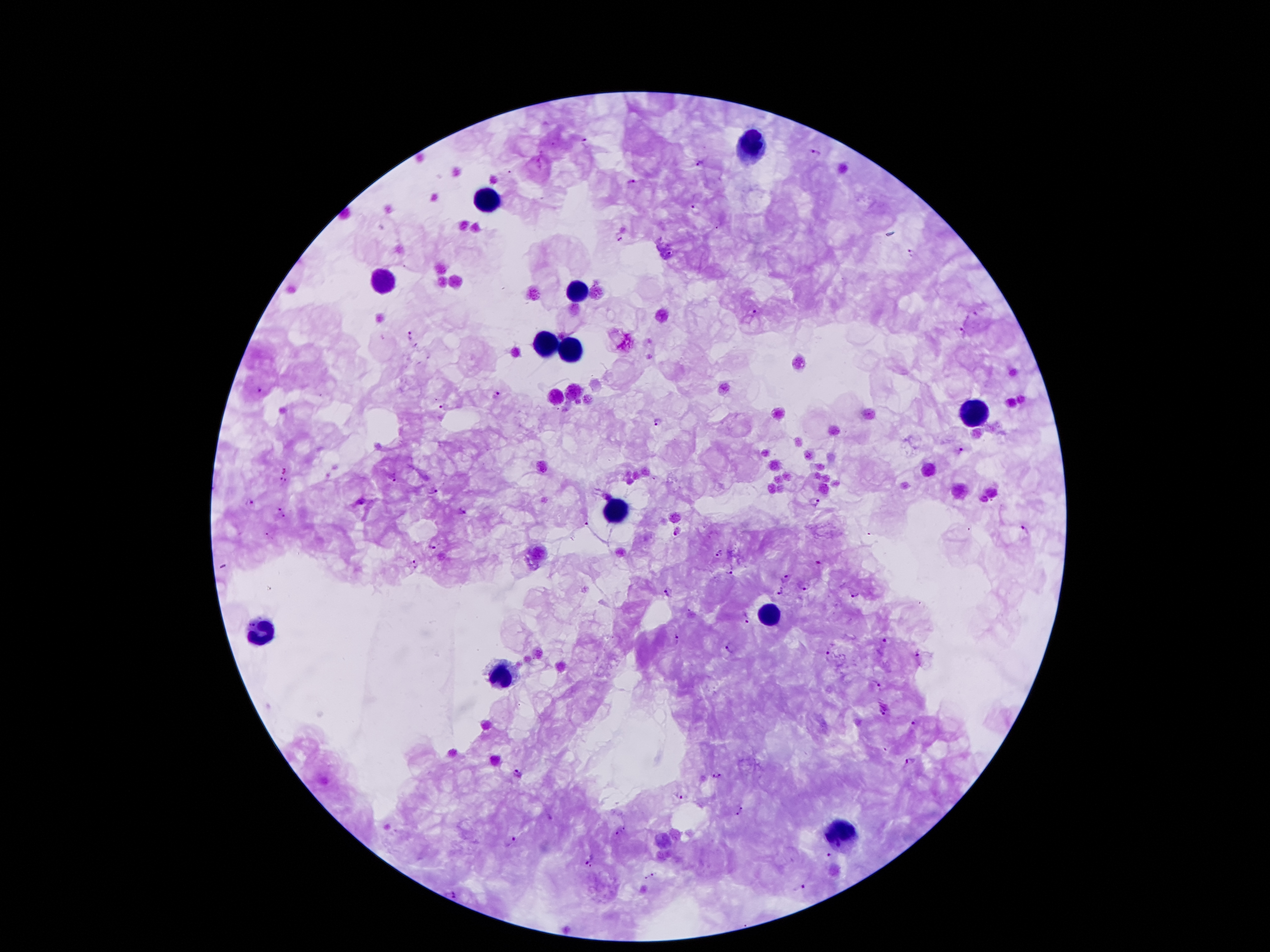
{
  "capture": "smartphone camera through the microscope eyepiece",
  "image_size": "1270×952 pixels",
  "plasmodium_parasite_locations": "approximate centers as (x, y) in pixels: (587, 140), (815, 152), (698, 163), (632, 182), (695, 207), (621, 238), (914, 250), (669, 253), (755, 314), (977, 314), (962, 331), (411, 334), (258, 388), (498, 395), (440, 406), (656, 421), (961, 449), (393, 478), (282, 481), (432, 491), (251, 502), (816, 502), (278, 507), (464, 512), (285, 517), (588, 525), (1025, 528), (678, 530), (269, 533), (432, 546), (718, 552), (818, 561), (416, 565), (732, 572), (784, 578), (803, 586), (668, 592), (779, 592), (855, 595), (748, 622), (677, 639), (885, 640), (729, 646), (828, 652), (918, 653), (878, 685), (884, 710), (915, 722), (911, 760), (518, 773), (717, 775), (680, 795), (743, 807), (736, 814), (551, 817), (618, 832), (511, 840), (829, 855), (585, 858), (590, 866), (655, 873), (646, 877), (803, 886), (454, 894)",
  "magnification": "100x",
  "patient_malaria_status": "positive for Plasmodium falciparum",
  "leukocyte_locations": "approximate centers as (x, y) in pixels: (750, 146), (485, 197), (385, 281), (577, 285), (547, 343), (575, 349), (977, 410), (612, 509), (770, 611), (262, 628), (499, 673), (840, 830)",
  "field_of_view": "single",
  "stain": "Giemsa",
  "preparation": "thick blood film"
}